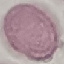
malaria_status: uninfected
image_type: automatically extracted cell patch, resized to 64 × 64 pixels
stain: Giemsa
preparation: thin blood film
capture: smartphone camera at the microscope eyepiece